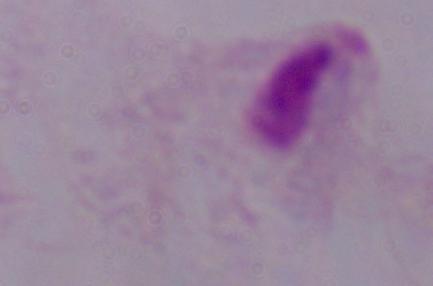
identification = trichomonad
magnification = 1000x
modality = photomicrograph